Locate and identify every blood parasite.
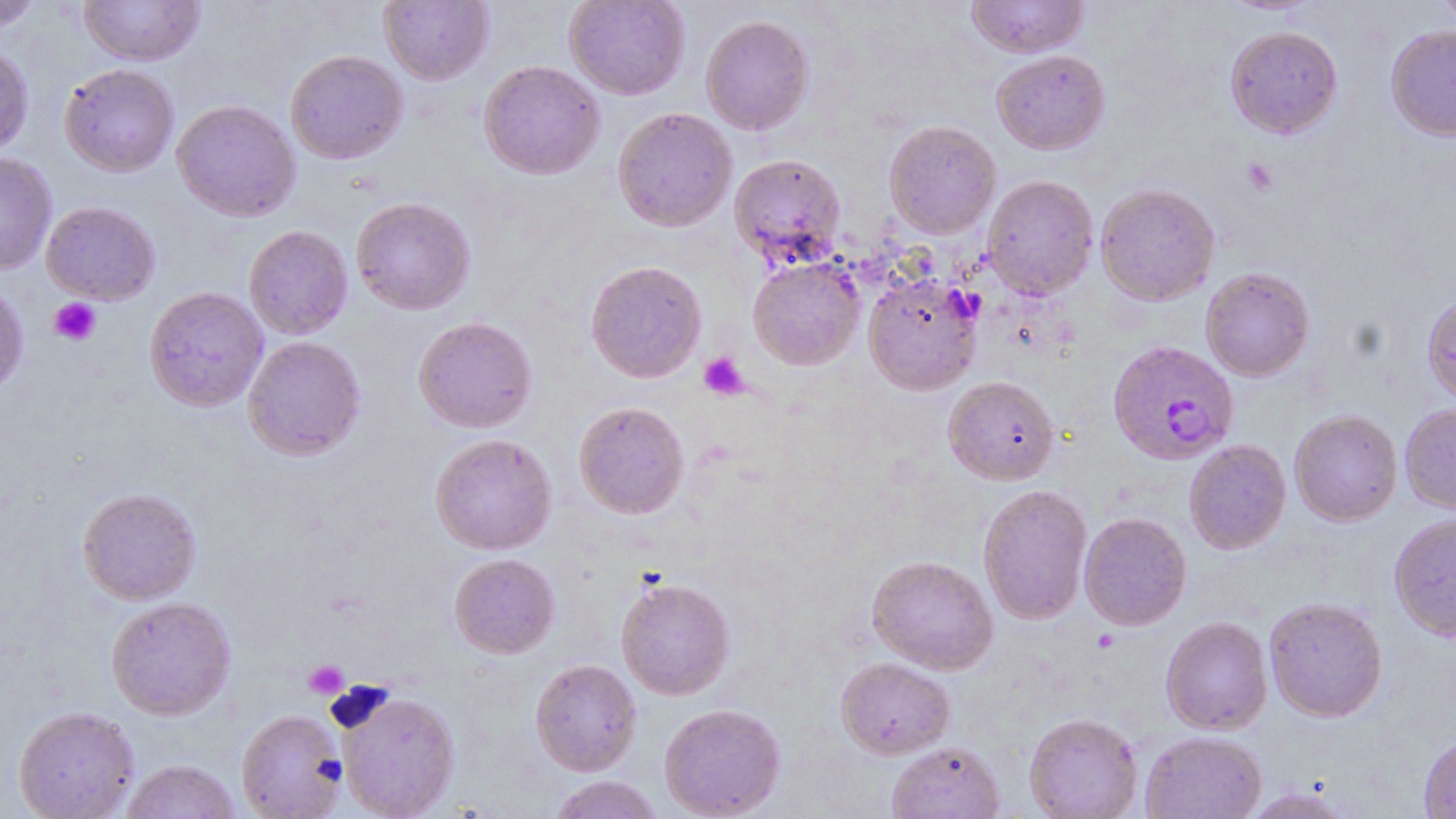

Approximate bounding boxes as (x1, y1, x2, y2) in pixels.
Plasmodium falciparum-infected red blood cells: (1108, 340, 1239, 465).
No Plasmodium ovale, Plasmodium malariae, Plasmodium vivax, Babesia divergens, or Trypanosoma brucei observed.

Summary:
  - Uninfected red blood cell locations: (79, 0, 205, 66), (379, 0, 493, 85), (564, 0, 690, 100), (966, 0, 1089, 57), (1436, 0, 1456, 33), (0, 1, 44, 31), (700, 14, 814, 135), (1386, 24, 1456, 141), (1225, 25, 1343, 138), (0, 43, 34, 158), (285, 49, 408, 164), (991, 50, 1110, 154), (478, 60, 605, 180), (59, 63, 179, 177), (172, 99, 300, 222), (612, 107, 737, 232), (884, 121, 1001, 239), (0, 153, 57, 275), (728, 153, 846, 268), (982, 174, 1099, 300), (1095, 183, 1220, 305), (351, 197, 476, 315), (41, 201, 160, 305), (244, 225, 352, 339), (748, 256, 865, 370), (585, 260, 707, 383), (1201, 266, 1315, 381), (863, 274, 983, 395), (0, 282, 28, 397), (144, 286, 268, 412), (1422, 291, 1456, 408), (413, 316, 537, 433), (243, 336, 365, 460), (943, 375, 1059, 485), (574, 401, 690, 519), (1399, 403, 1456, 514), (1289, 409, 1403, 526), (430, 433, 556, 554), (1184, 439, 1291, 554), (978, 484, 1093, 625), (77, 487, 201, 605), (1079, 511, 1192, 630), (1389, 513, 1456, 641), (449, 553, 560, 658), (867, 555, 998, 674), (615, 576, 735, 700), (105, 596, 236, 720), (1264, 596, 1388, 722), (1161, 616, 1273, 734), (836, 656, 955, 758), (530, 659, 642, 776), (336, 689, 460, 819), (659, 702, 786, 819), (13, 705, 139, 818), (236, 709, 348, 818), (1024, 712, 1143, 818), (1141, 730, 1267, 819), (1419, 733, 1456, 818), (886, 741, 1004, 818), (120, 759, 241, 819), (548, 775, 663, 819), (1238, 786, 1357, 818)
  - Platelet locations: (1241, 157, 1278, 195), (49, 297, 101, 345), (698, 351, 749, 400), (304, 660, 349, 699)
  - Slide-level diagnosis: Plasmodium falciparum
  - Modality: light microscopy
  - Stain: May-Grünwald-Giemsa
  - Field of view: single
  - Magnification: 1000x
  - Preparation: thin blood film
  - Image size: 1456×819 pixels